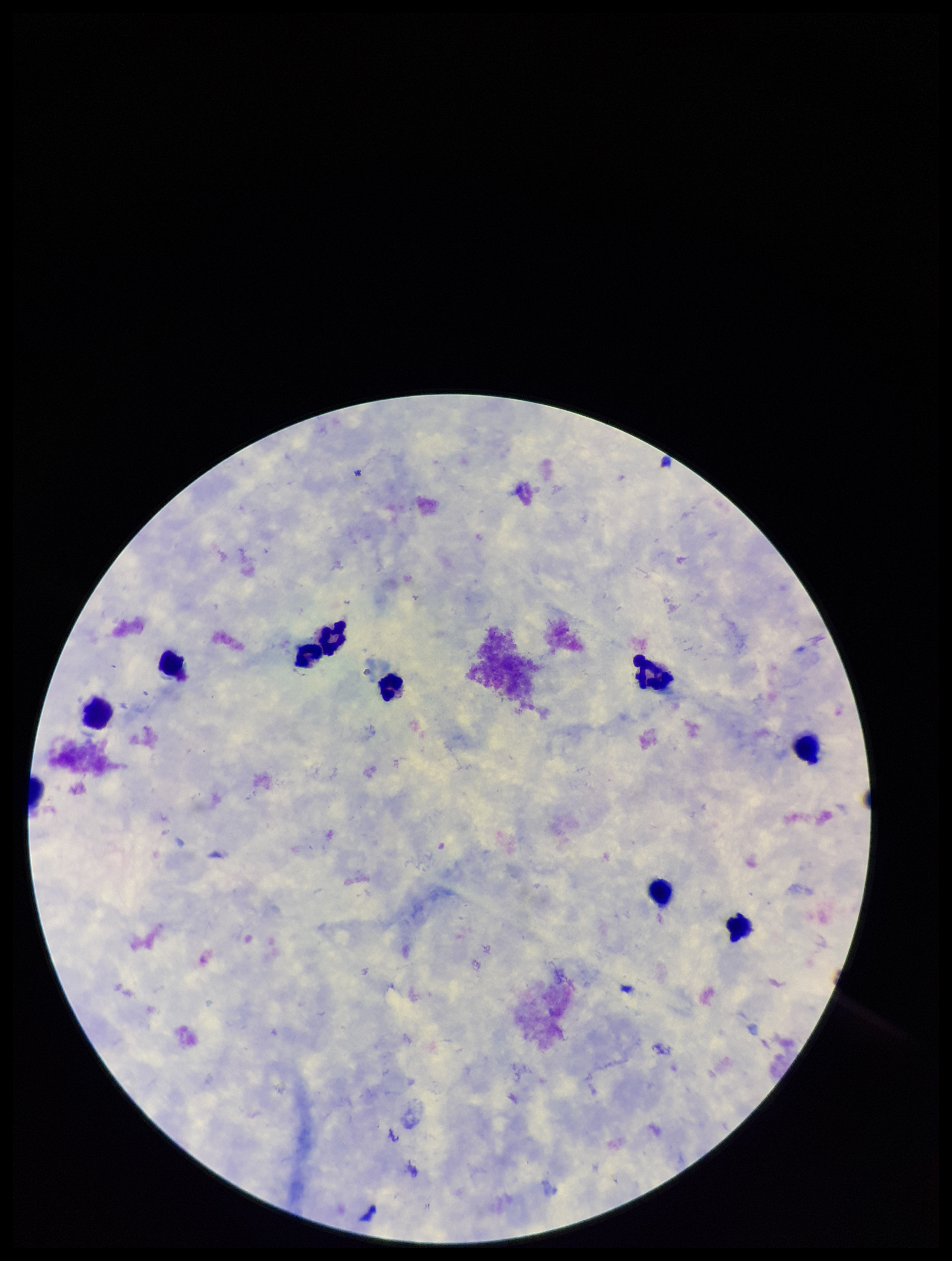
{
  "stain": "Giemsa",
  "patient_malaria_status": "negative",
  "preparation": "thick smear",
  "leukocyte_count": 10,
  "image_size": "952×1261 pixels",
  "field_of_view": "single",
  "capture": "smartphone photograph through the microscope eyepiece",
  "parasite_count": 0,
  "plasmodium_parasites": "none detected"
}